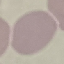
Summary:
  - Malaria status: uninfected
  - Capture: smartphone through the microscope eyepiece
  - Stain: Giemsa
  - Preparation: thin blood smear
  - Image type: automatically extracted cell patch, resized to 64 × 64 pixels